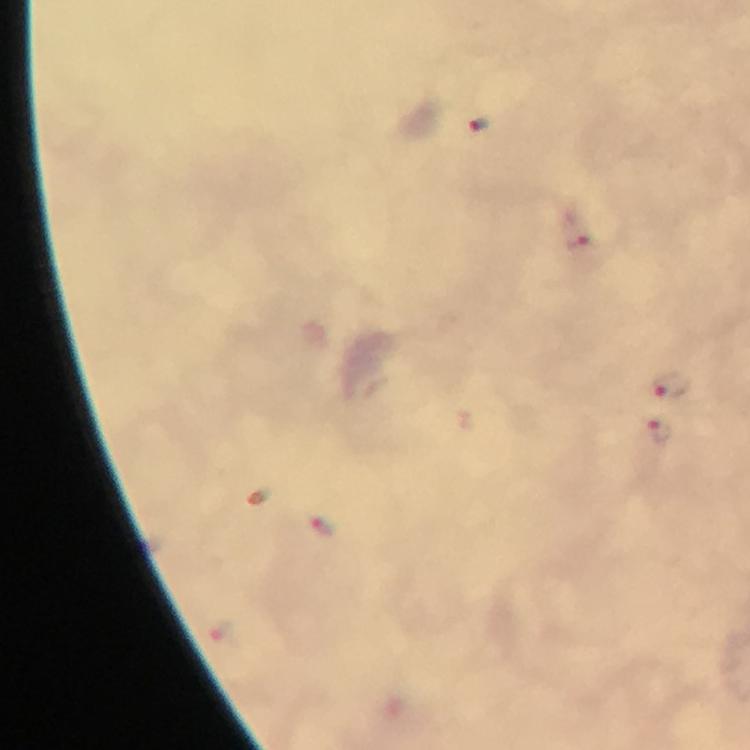

Approximate centers as (x, y) in pixels.
Summary:
  - Plasmodium parasite locations: (478, 125), (579, 232), (670, 384), (662, 432), (325, 527)
  - Preparation: thick blood smear
  - Capture: smartphone photograph through a microscope
  - Immersion oil: used
  - Magnification: 100x
  - Context: from a diagnostic examination for malaria
  - Cropped from: one field of view
  - Image size: 750×750 pixels
  - Stain: Giemsa